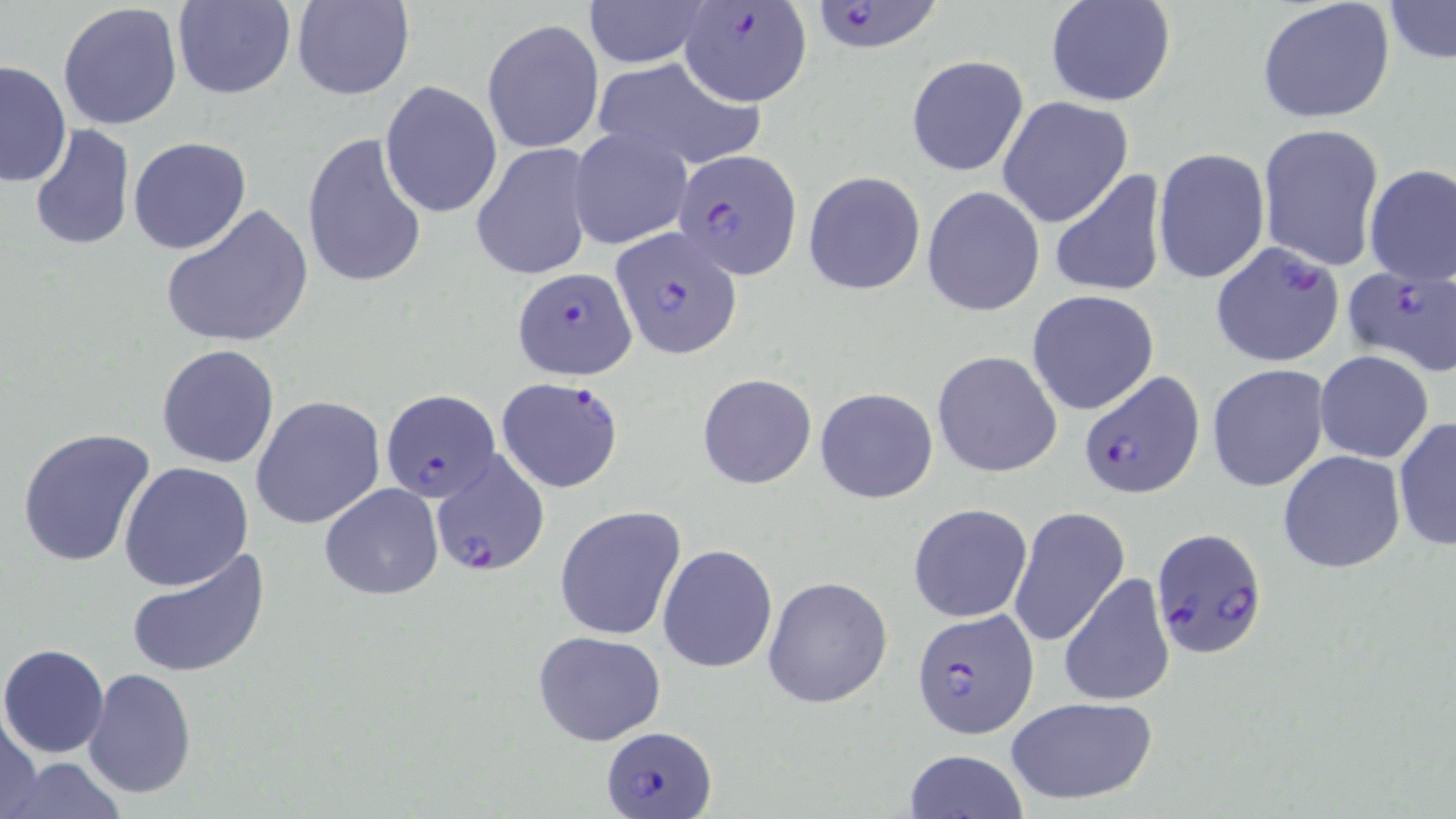
{
  "slide_level_diagnosis": "Plasmodium falciparum",
  "field_of_view": "one of a larger specimen",
  "preparation": "thin blood film",
  "plasmodium_falciparum_infected_red_blood_cell_locations": "approximate bounding boxes as (x1,y1)-(x2,y2) corner pairs in pixels: (806,0)-(949,54), (677,4)-(811,108), (671,141)-(800,273), (609,228)-(742,359), (1209,241)-(1349,369), (1340,263)-(1456,380), (512,266)-(637,382), (1080,369)-(1205,499), (497,377)-(625,494), (379,390)-(500,503), (430,449)-(549,576), (1150,525)-(1270,660), (911,609)-(1038,738), (601,724)-(719,816)",
  "image_size": "1456×819 pixels",
  "uninfected_red_blood_cell_locations": "approximate bounding boxes as (x1,y1)-(x2,y2) corner pairs in pixels: (174,0)-(294,99), (291,0)-(414,101), (1048,0)-(1176,106), (1257,0)-(1396,125), (1381,0)-(1455,63), (584,1)-(709,68), (58,3)-(184,132), (482,19)-(603,154), (906,56)-(1029,177), (586,57)-(764,172), (1,59)-(73,188), (379,80)-(503,218), (997,96)-(1133,227), (1256,122)-(1385,270), (29,124)-(134,250), (569,127)-(693,250), (302,131)-(429,292), (129,137)-(252,255), (472,143)-(596,281), (1152,147)-(1270,284), (1362,165)-(1456,286), (1047,170)-(1167,299), (803,171)-(926,295), (922,186)-(1045,317), (162,201)-(314,349), (1026,290)-(1159,415), (156,343)-(281,468), (932,350)-(1062,478), (1315,351)-(1433,463), (1207,364)-(1330,491), (699,373)-(817,488), (814,388)-(938,504), (251,395)-(385,529), (1392,415)-(1456,553), (16,425)-(157,567), (1278,449)-(1405,574), (119,462)-(255,590), (320,483)-(443,600), (909,503)-(1033,622), (555,505)-(687,641), (1006,507)-(1128,650), (658,544)-(778,672), (125,547)-(271,679), (1059,573)-(1176,707), (763,576)-(892,707), (533,630)-(667,746), (0,643)-(109,758), (82,668)-(197,797), (1003,695)-(1157,806), (0,709)-(45,819), (903,749)-(1029,819), (4,757)-(127,817)",
  "stain": "May-Grünwald-Giemsa",
  "modality": "light microscopy",
  "magnification": "1000x"
}